Locate every blood parasite and identify its species.
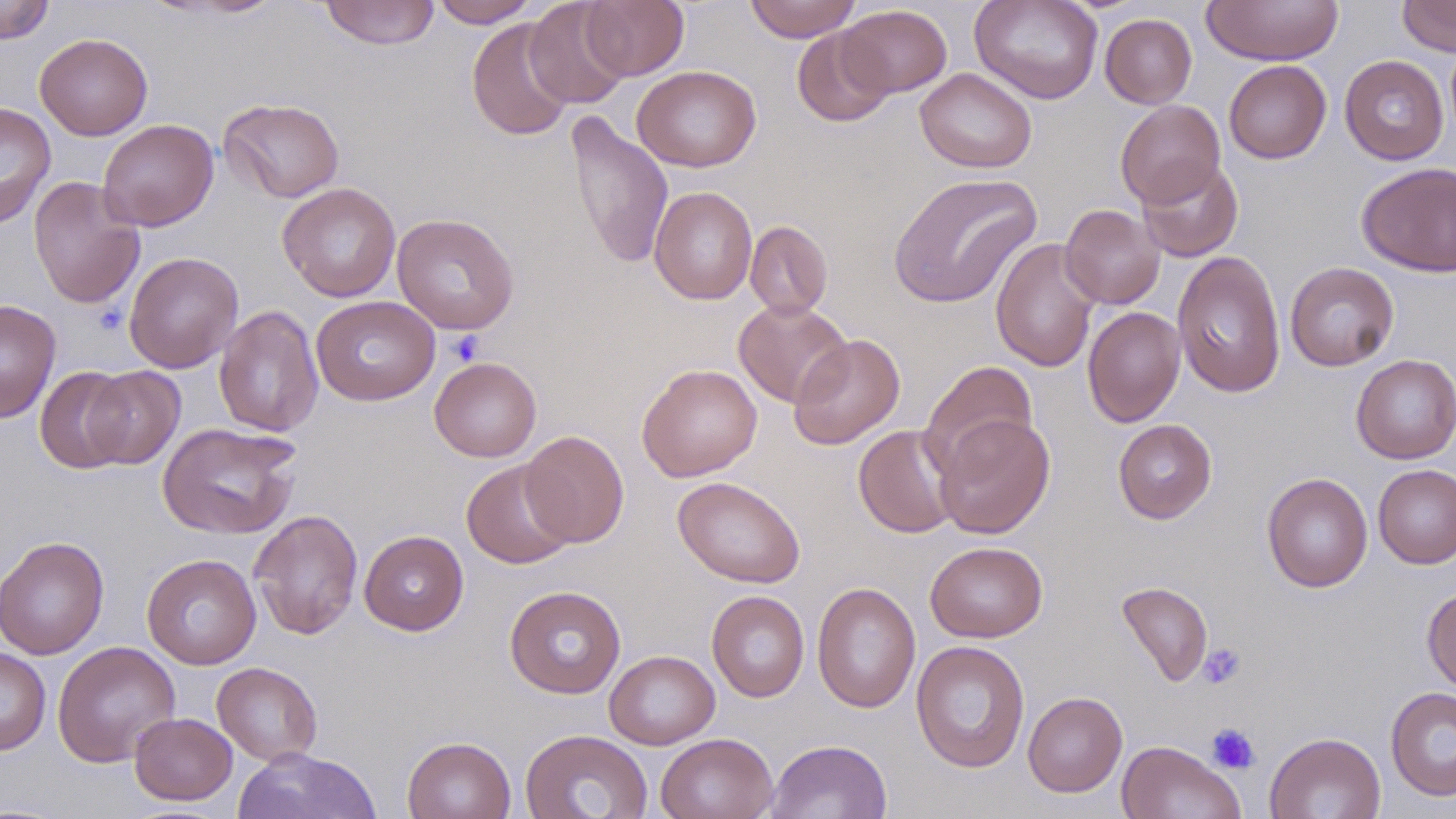
No blood parasites observed.

Summary:
  - Coordinate format: approximate bounding boxes as named x1/y1/x2/y2 corners in pixels
  - Platelet locations: (x1=446, y1=331, x2=485, y2=366), (x1=1197, y1=642, x2=1246, y2=689), (x1=1206, y1=723, x2=1260, y2=774)
  - Uninfected red blood cell locations: (x1=320, y1=0, x2=439, y2=50), (x1=430, y1=0, x2=540, y2=28), (x1=524, y1=0, x2=632, y2=109), (x1=581, y1=0, x2=690, y2=80), (x1=744, y1=0, x2=861, y2=42), (x1=969, y1=0, x2=1104, y2=104), (x1=1201, y1=0, x2=1344, y2=66), (x1=1397, y1=0, x2=1456, y2=56), (x1=0, y1=1, x2=55, y2=44), (x1=838, y1=5, x2=952, y2=98), (x1=1100, y1=13, x2=1197, y2=109), (x1=466, y1=17, x2=576, y2=141), (x1=792, y1=28, x2=895, y2=127), (x1=35, y1=33, x2=153, y2=140), (x1=1339, y1=54, x2=1449, y2=165), (x1=1224, y1=60, x2=1331, y2=164), (x1=632, y1=65, x2=761, y2=172), (x1=915, y1=67, x2=1037, y2=173), (x1=219, y1=98, x2=345, y2=202), (x1=1115, y1=99, x2=1226, y2=209), (x1=0, y1=102, x2=56, y2=229), (x1=565, y1=110, x2=674, y2=270), (x1=97, y1=119, x2=219, y2=232), (x1=1136, y1=158, x2=1244, y2=262), (x1=1357, y1=162, x2=1456, y2=276), (x1=887, y1=172, x2=1042, y2=309), (x1=28, y1=176, x2=145, y2=310), (x1=277, y1=182, x2=401, y2=302), (x1=649, y1=186, x2=758, y2=305), (x1=1059, y1=204, x2=1165, y2=310), (x1=391, y1=213, x2=519, y2=335), (x1=745, y1=220, x2=833, y2=319), (x1=990, y1=237, x2=1101, y2=373), (x1=123, y1=251, x2=243, y2=373), (x1=1172, y1=251, x2=1286, y2=398), (x1=1285, y1=261, x2=1400, y2=371), (x1=311, y1=295, x2=440, y2=405), (x1=0, y1=299, x2=61, y2=424), (x1=733, y1=299, x2=852, y2=408), (x1=213, y1=304, x2=324, y2=437), (x1=1083, y1=306, x2=1185, y2=428), (x1=788, y1=333, x2=906, y2=450), (x1=1350, y1=354, x2=1456, y2=464), (x1=429, y1=357, x2=541, y2=462), (x1=920, y1=361, x2=1038, y2=476), (x1=636, y1=363, x2=763, y2=482), (x1=35, y1=366, x2=135, y2=474), (x1=82, y1=366, x2=185, y2=469), (x1=934, y1=413, x2=1055, y2=539), (x1=1113, y1=419, x2=1217, y2=523), (x1=157, y1=421, x2=302, y2=540), (x1=854, y1=424, x2=962, y2=538), (x1=520, y1=430, x2=629, y2=548), (x1=461, y1=459, x2=576, y2=569), (x1=1373, y1=463, x2=1456, y2=569), (x1=1261, y1=472, x2=1373, y2=593), (x1=673, y1=476, x2=805, y2=589), (x1=249, y1=509, x2=363, y2=640), (x1=359, y1=530, x2=468, y2=635), (x1=0, y1=535, x2=109, y2=660), (x1=925, y1=541, x2=1047, y2=642), (x1=142, y1=553, x2=261, y2=669), (x1=1116, y1=581, x2=1213, y2=687), (x1=811, y1=582, x2=921, y2=713), (x1=504, y1=585, x2=626, y2=699), (x1=1422, y1=586, x2=1456, y2=696), (x1=707, y1=590, x2=810, y2=702), (x1=911, y1=640, x2=1030, y2=773), (x1=52, y1=641, x2=181, y2=767), (x1=0, y1=647, x2=51, y2=755), (x1=605, y1=650, x2=720, y2=750), (x1=212, y1=662, x2=323, y2=766), (x1=1386, y1=686, x2=1456, y2=801), (x1=1022, y1=691, x2=1127, y2=797), (x1=129, y1=712, x2=237, y2=806), (x1=519, y1=728, x2=653, y2=819), (x1=1264, y1=731, x2=1386, y2=819), (x1=655, y1=732, x2=778, y2=819), (x1=402, y1=735, x2=516, y2=819), (x1=765, y1=739, x2=892, y2=819), (x1=1116, y1=740, x2=1246, y2=819), (x1=232, y1=747, x2=381, y2=819)
  - Slide-level diagnosis: negative for blood parasites
  - Field of view: one of a larger specimen
  - Magnification: 1000x
  - Modality: optical microscopy
  - Preparation: thin blood film
  - Image size: 1456×819 pixels
  - Stain: May-Grünwald-Giemsa